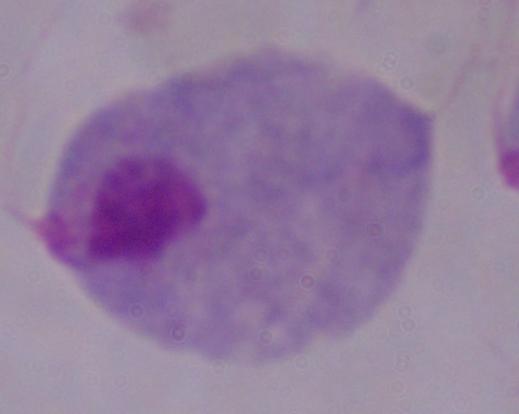

Summary:
  - Modality: photomicrograph
  - Magnification: 1000x
  - Identification: trichomonad